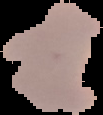

preparation: thin blood film
malaria_status: parasitized
image_size: 103×115 pixels
image_type: cell region segmented out of the field of view; surrounding area masked to black